Comment on the morphology of the erythrocytes.
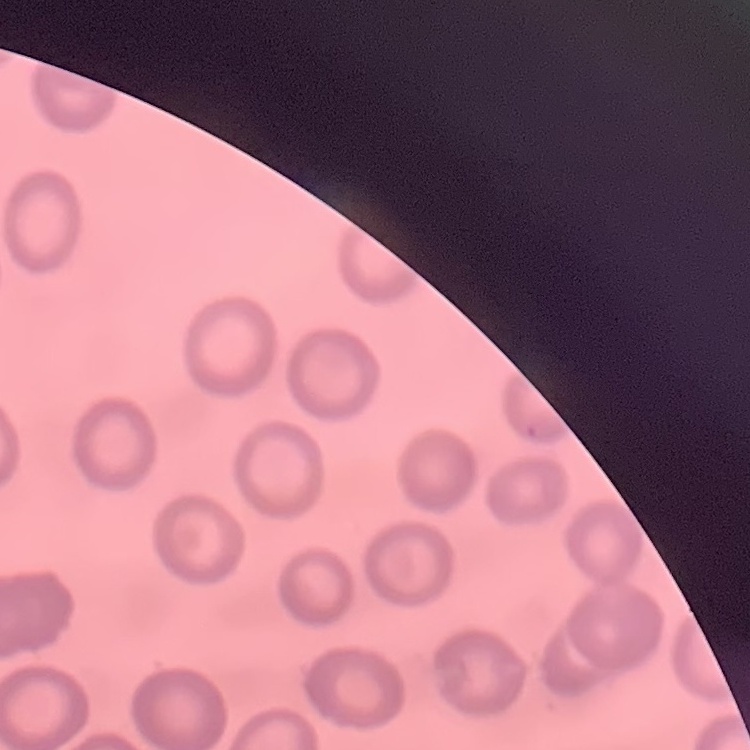

No rouleaux formation.

stain = Field's or Giemsa
preparation = thin blood film
image type = one tile cut from a larger photomicrograph